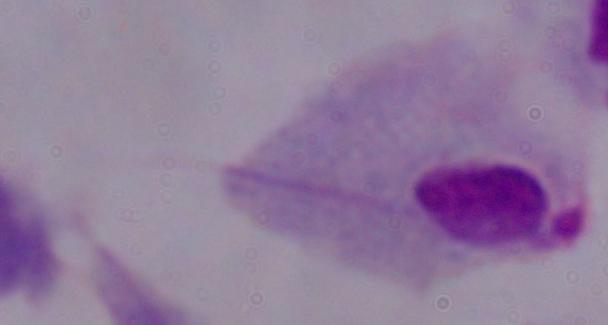

Summary:
  - Identification: trichomonad
  - Modality: micrograph
  - Magnification: 1000x